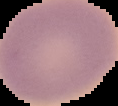
{
  "image_size": "118×106 pixels",
  "malaria_status": "uninfected",
  "image_type": "cell region segmented out of the field of view; surrounding area masked to black",
  "preparation": "thin blood smear"
}